Describe the morphology of the red blood cells.
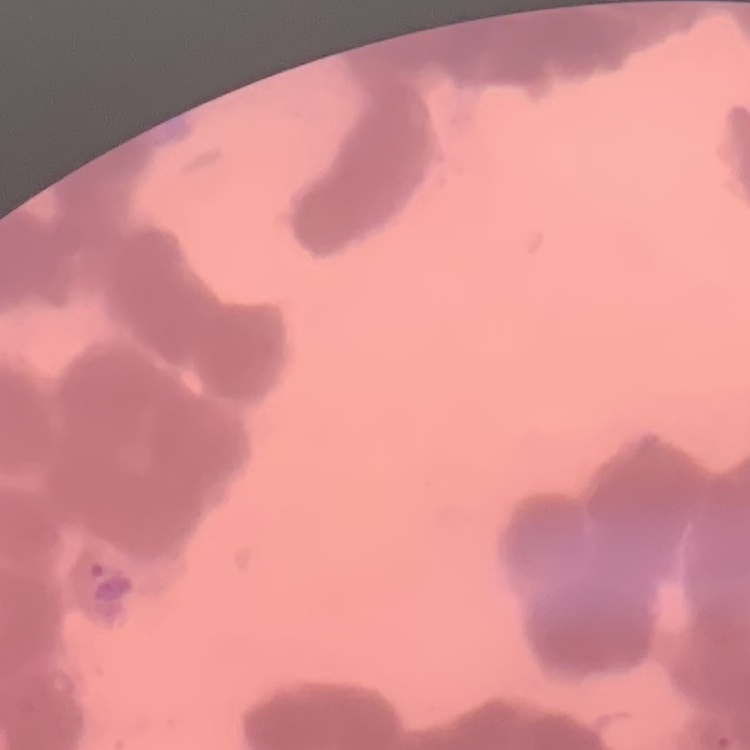

Rouleaux formation.

Summary:
  - Preparation: thin peripheral smear
  - Stain: Field's or Giemsa
  - Image type: one tile cut from a larger photomicrograph